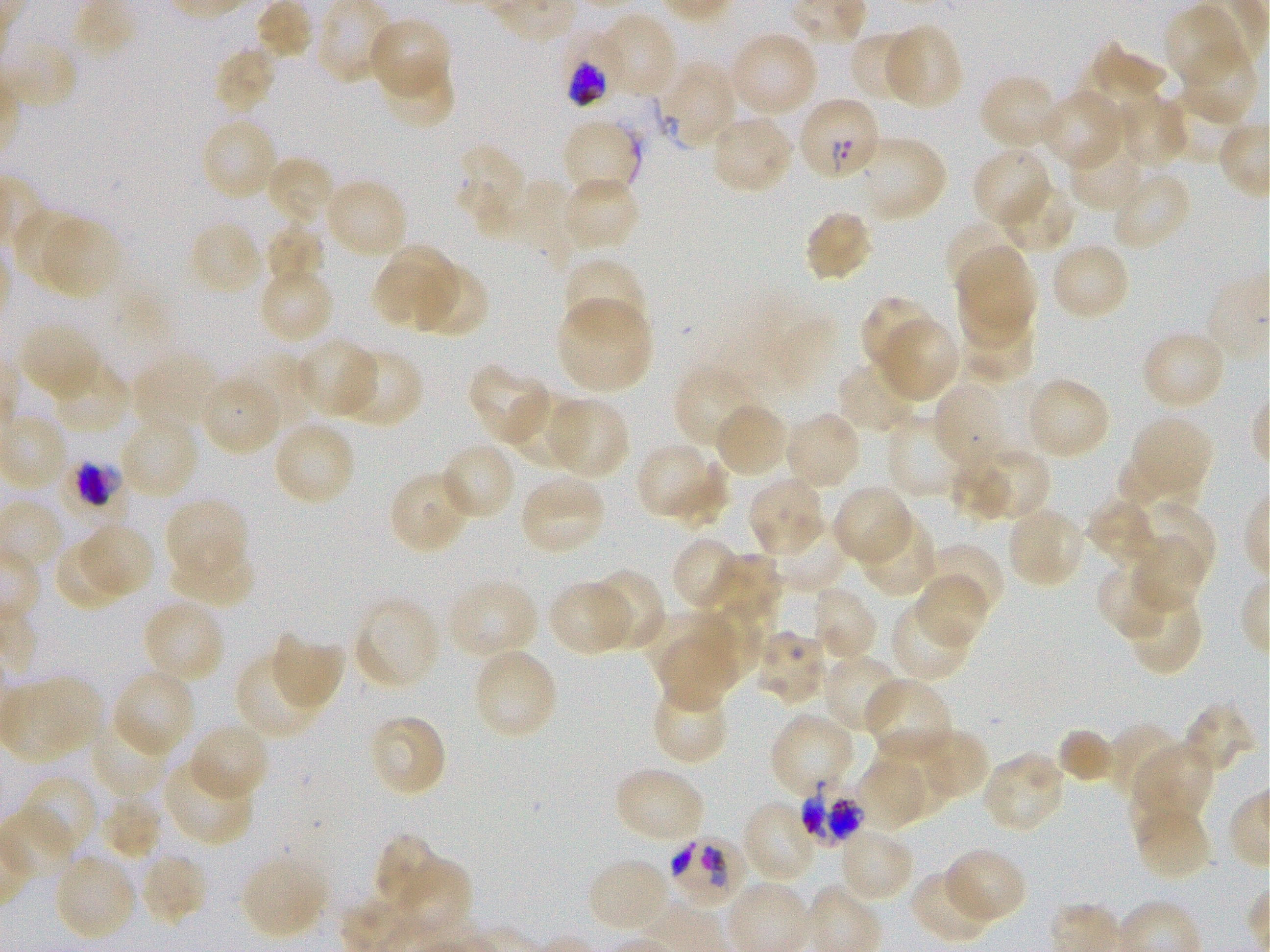
Approximate bounding rectangles given as corner coordinates in pixels from the top-left. Not every red blood cell is marked. A life-cycle stage — or a range of stages, where the recorded stages span more than one — follows each staged infected red blood cell. Locations of uninfected red blood cells: (x1=256, y1=0, x2=312, y2=60), (x1=1164, y1=4, x2=1245, y2=87), (x1=597, y1=13, x2=679, y2=101), (x1=366, y1=18, x2=451, y2=102), (x1=882, y1=23, x2=964, y2=111), (x1=728, y1=29, x2=820, y2=119), (x1=849, y1=31, x2=924, y2=107), (x1=1181, y1=42, x2=1260, y2=125), (x1=1079, y1=45, x2=1172, y2=135), (x1=213, y1=46, x2=278, y2=115), (x1=378, y1=60, x2=456, y2=130), (x1=659, y1=62, x2=737, y2=150), (x1=978, y1=74, x2=1062, y2=151), (x1=1165, y1=88, x2=1249, y2=166), (x1=1038, y1=89, x2=1126, y2=172), (x1=1111, y1=94, x2=1189, y2=170), (x1=709, y1=116, x2=794, y2=196), (x1=199, y1=117, x2=280, y2=203), (x1=561, y1=118, x2=640, y2=201), (x1=1065, y1=130, x2=1148, y2=213), (x1=851, y1=135, x2=947, y2=222), (x1=453, y1=141, x2=530, y2=240), (x1=971, y1=147, x2=1053, y2=231), (x1=265, y1=154, x2=337, y2=230), (x1=1110, y1=170, x2=1192, y2=252), (x1=561, y1=175, x2=640, y2=254), (x1=323, y1=178, x2=409, y2=261), (x1=483, y1=180, x2=575, y2=269), (x1=1000, y1=180, x2=1076, y2=255), (x1=10, y1=208, x2=91, y2=291), (x1=803, y1=209, x2=874, y2=283), (x1=39, y1=215, x2=122, y2=302), (x1=946, y1=218, x2=1024, y2=300), (x1=188, y1=220, x2=265, y2=297), (x1=264, y1=223, x2=324, y2=288), (x1=1050, y1=240, x2=1131, y2=321), (x1=388, y1=244, x2=460, y2=315), (x1=956, y1=247, x2=1039, y2=331), (x1=562, y1=256, x2=646, y2=341), (x1=408, y1=260, x2=488, y2=337), (x1=952, y1=262, x2=1044, y2=349), (x1=372, y1=264, x2=449, y2=330), (x1=262, y1=271, x2=333, y2=339), (x1=859, y1=295, x2=939, y2=377), (x1=555, y1=296, x2=654, y2=395), (x1=956, y1=313, x2=1037, y2=385), (x1=878, y1=316, x2=960, y2=403), (x1=19, y1=321, x2=103, y2=400), (x1=1140, y1=329, x2=1228, y2=412), (x1=295, y1=338, x2=379, y2=420), (x1=335, y1=348, x2=423, y2=429), (x1=133, y1=352, x2=223, y2=434), (x1=235, y1=352, x2=316, y2=427), (x1=48, y1=360, x2=131, y2=434), (x1=836, y1=360, x2=921, y2=436), (x1=468, y1=364, x2=556, y2=447), (x1=674, y1=364, x2=760, y2=452), (x1=1023, y1=376, x2=1110, y2=461), (x1=199, y1=379, x2=279, y2=451), (x1=932, y1=381, x2=1011, y2=474), (x1=507, y1=393, x2=584, y2=470), (x1=543, y1=397, x2=628, y2=479), (x1=712, y1=402, x2=789, y2=480), (x1=782, y1=410, x2=862, y2=491), (x1=885, y1=415, x2=967, y2=500), (x1=1132, y1=415, x2=1214, y2=493), (x1=119, y1=416, x2=201, y2=500), (x1=271, y1=420, x2=357, y2=508), (x1=440, y1=441, x2=518, y2=521), (x1=635, y1=442, x2=711, y2=518), (x1=979, y1=447, x2=1050, y2=521), (x1=667, y1=450, x2=742, y2=534), (x1=1115, y1=454, x2=1201, y2=514), (x1=947, y1=456, x2=1012, y2=529), (x1=389, y1=470, x2=474, y2=556), (x1=518, y1=474, x2=608, y2=557), (x1=746, y1=476, x2=827, y2=557), (x1=831, y1=484, x2=914, y2=567), (x1=165, y1=497, x2=249, y2=584), (x1=1085, y1=497, x2=1159, y2=569), (x1=1005, y1=506, x2=1087, y2=590), (x1=1139, y1=506, x2=1215, y2=581), (x1=858, y1=514, x2=936, y2=597), (x1=779, y1=521, x2=850, y2=589), (x1=85, y1=524, x2=153, y2=594), (x1=671, y1=534, x2=746, y2=612), (x1=1129, y1=534, x2=1207, y2=613), (x1=55, y1=540, x2=126, y2=609), (x1=922, y1=541, x2=1004, y2=623), (x1=171, y1=548, x2=258, y2=603), (x1=704, y1=555, x2=782, y2=632), (x1=1097, y1=563, x2=1176, y2=641), (x1=588, y1=569, x2=665, y2=652), (x1=913, y1=573, x2=991, y2=650), (x1=452, y1=579, x2=539, y2=654), (x1=548, y1=580, x2=634, y2=657), (x1=810, y1=584, x2=879, y2=665), (x1=1124, y1=586, x2=1203, y2=676), (x1=353, y1=596, x2=442, y2=691), (x1=142, y1=598, x2=227, y2=685), (x1=889, y1=599, x2=974, y2=681), (x1=641, y1=609, x2=715, y2=684), (x1=692, y1=611, x2=764, y2=686), (x1=754, y1=628, x2=830, y2=706), (x1=269, y1=633, x2=344, y2=713), (x1=658, y1=642, x2=733, y2=712), (x1=234, y1=651, x2=322, y2=741), (x1=477, y1=652, x2=554, y2=738), (x1=822, y1=653, x2=905, y2=735), (x1=111, y1=667, x2=195, y2=759), (x1=4, y1=676, x2=103, y2=762), (x1=864, y1=676, x2=953, y2=761), (x1=650, y1=682, x2=728, y2=765), (x1=1182, y1=701, x2=1255, y2=776), (x1=769, y1=711, x2=858, y2=796), (x1=367, y1=714, x2=448, y2=798), (x1=88, y1=716, x2=173, y2=801), (x1=187, y1=721, x2=270, y2=804), (x1=1106, y1=721, x2=1181, y2=801), (x1=1056, y1=727, x2=1120, y2=784), (x1=911, y1=728, x2=989, y2=802), (x1=868, y1=730, x2=960, y2=814), (x1=1132, y1=742, x2=1216, y2=824), (x1=981, y1=751, x2=1068, y2=833), (x1=855, y1=754, x2=933, y2=832), (x1=162, y1=757, x2=254, y2=846), (x1=612, y1=765, x2=707, y2=844), (x1=22, y1=775, x2=99, y2=857), (x1=100, y1=792, x2=162, y2=860), (x1=740, y1=799, x2=820, y2=885), (x1=1130, y1=801, x2=1212, y2=881), (x1=837, y1=828, x2=915, y2=904), (x1=376, y1=835, x2=439, y2=911), (x1=942, y1=847, x2=1027, y2=925), (x1=137, y1=851, x2=209, y2=926), (x1=241, y1=853, x2=329, y2=939), (x1=400, y1=855, x2=472, y2=938), (x1=586, y1=857, x2=672, y2=936), (x1=57, y1=859, x2=134, y2=937), (x1=910, y1=868, x2=997, y2=944). Locations of infected red blood cells: (x1=558, y1=33, x2=623, y2=107) early schizont; (x1=796, y1=95, x2=881, y2=182); (x1=58, y1=463, x2=131, y2=532) early schizont; (x1=799, y1=776, x2=867, y2=844); (x1=665, y1=833, x2=746, y2=908). P. falciparum strain 3D7 maintained in static in-vitro culture. Giemsa stain. Thin blood smear. Oil immersion, 100x objective (numerical aperture 1.25). Donor blood group O+. One field from this slide. Image is 1270×952 pixels.